State which cell type is depicted.
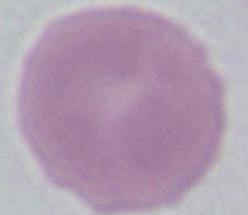
An erythrocyte.

Summary:
  - Magnification: 1000x
  - Modality: micrograph